Mark where platelets are.
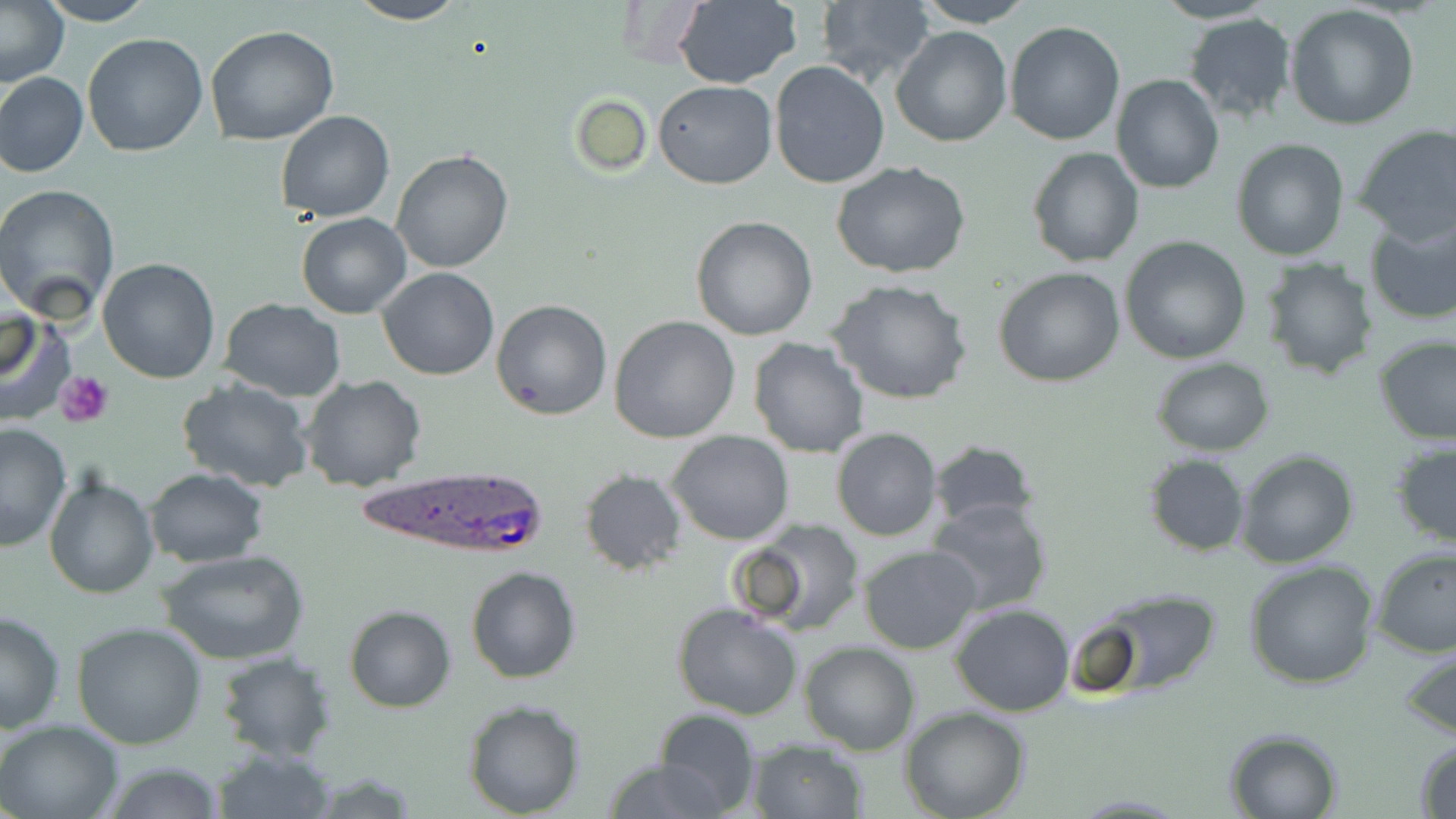

Approximate bounding boxes as (x1, y1, x2, y2) in pixels.
Platelets: (57, 370, 113, 427).

Plasmodium ovale-infected red blood cell locations: (350, 465, 549, 562). Uninfected red blood cell locations: (36, 0, 159, 25), (346, 0, 467, 25), (673, 0, 802, 88), (814, 0, 936, 90), (913, 0, 1038, 27), (1151, 0, 1280, 25), (0, 1, 70, 88), (1285, 6, 1420, 131), (1182, 14, 1299, 124), (1005, 21, 1126, 146), (206, 24, 340, 146), (892, 26, 1013, 147), (81, 32, 208, 157), (769, 62, 889, 189), (0, 71, 88, 178), (1110, 74, 1225, 194), (653, 81, 777, 188), (570, 92, 652, 178), (276, 110, 395, 222), (1353, 123, 1456, 245), (1231, 137, 1349, 260), (1027, 146, 1144, 266), (391, 148, 515, 274), (830, 162, 972, 280), (0, 183, 120, 321), (297, 212, 412, 319), (1363, 213, 1456, 326), (691, 216, 818, 339), (1118, 235, 1251, 365), (1257, 256, 1379, 379), (97, 257, 222, 383), (377, 267, 500, 380), (994, 267, 1125, 387), (827, 278, 973, 406), (219, 297, 347, 402), (492, 300, 612, 420), (489, 306, 738, 426), (1, 307, 62, 419), (610, 315, 742, 443), (1373, 335, 1456, 445), (748, 337, 869, 458), (1151, 357, 1275, 455), (300, 375, 427, 493), (174, 378, 314, 493), (0, 422, 74, 553), (831, 428, 942, 542), (668, 430, 793, 545), (926, 438, 1041, 531), (1391, 441, 1456, 553), (1234, 450, 1360, 569), (1144, 454, 1251, 557), (144, 468, 267, 566), (579, 469, 687, 574), (44, 472, 159, 599), (925, 495, 1056, 618), (728, 520, 864, 637), (858, 544, 982, 655), (1371, 546, 1456, 658), (159, 549, 310, 665), (1244, 559, 1380, 688), (465, 566, 581, 683), (1078, 585, 1221, 693), (672, 601, 803, 720), (950, 603, 1075, 715), (343, 606, 455, 712), (0, 609, 66, 734), (71, 623, 208, 749), (799, 641, 921, 755), (1399, 644, 1456, 742), (213, 652, 337, 763), (463, 700, 586, 818), (902, 708, 1030, 819), (653, 709, 760, 817), (0, 718, 122, 819), (1223, 727, 1345, 818), (746, 738, 867, 818), (1413, 738, 1456, 819), (212, 744, 337, 818), (600, 758, 734, 817), (101, 759, 226, 818). Slide-level diagnosis: Plasmodium ovale. Thin blood film. Captured at 1000x magnification. Image is 1456×819 pixels. Single field of view. Light microscopy. May-Grünwald-Giemsa-stained preparation.